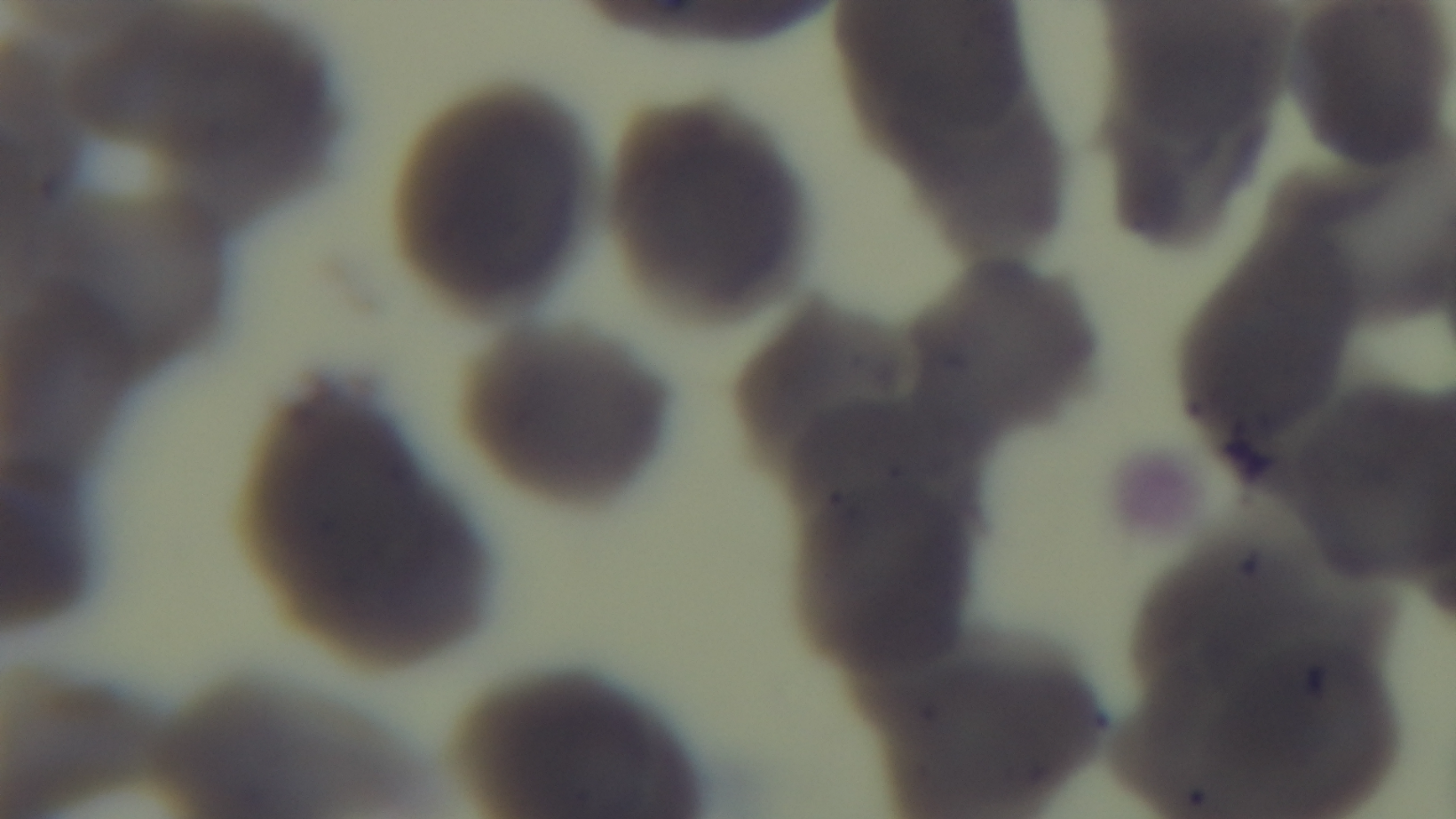
Mounted 4K digital camera. Light microscopy. Preparation: thin smear. Malaria status: uninfected. Single field of view. Oil-immersion objective, 100x. Giemsa-stained.